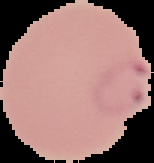
{
  "result": "malaria parasites identified",
  "preparation": "thin blood smear",
  "image_type": "cell region segmented out of the field of view; surrounding area masked to black",
  "image_size": "154×163 pixels"
}